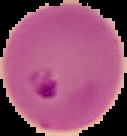
Image is 127×136 pixels. From a thin blood film. Segmented cell region on a black background. Result: malaria parasites identified.